Give the position of every Plasmodium parasite.
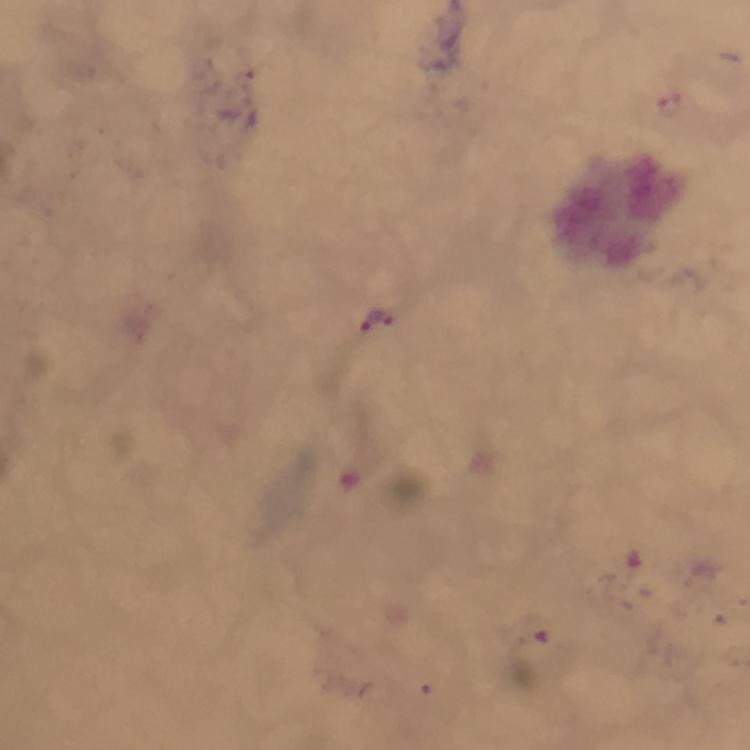
Approximate centers as (x, y) in pixels.
Plasmodium parasites: (378, 322).

Immersion oil applied. Photographed with a smartphone mounted on the microscope. Giemsa stain. 100x magnification. Image is 750×750 pixels. From a diagnostic examination for malaria. A crop from one field of view. Thick blood film.